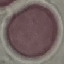

Result: no malaria parasites detected. Thin blood smear. Giemsa stain. Photographed with a smartphone camera at the microscope eyepiece. Automatically extracted cell patch, resized to 64 × 64 pixels.